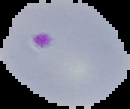
Image is 130×109 pixels. Malaria status: parasitized. Segmented cell region on a black background. From a thin blood smear.